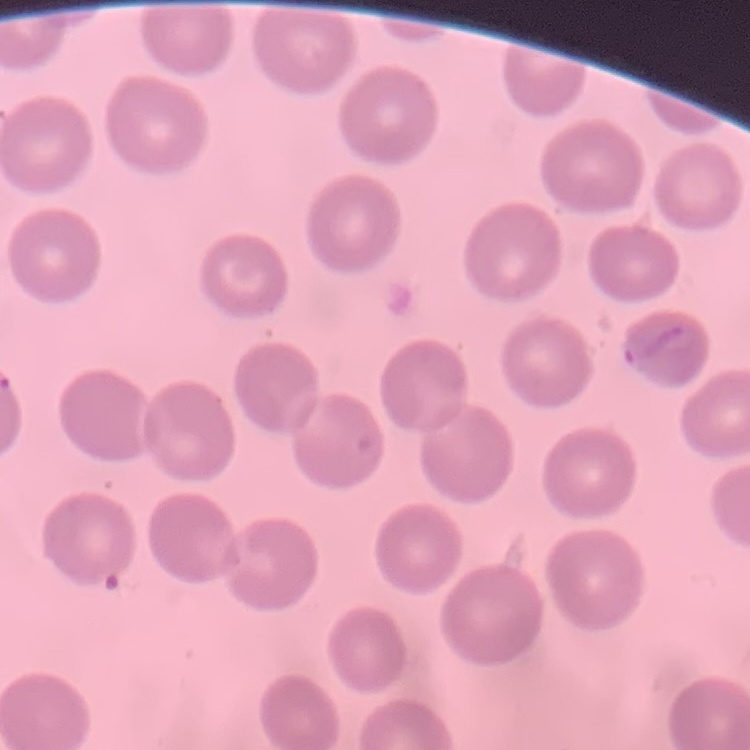
The erythrocytes exhibit no rouleaux formation. Thin blood film. One tile cut from a larger photomicrograph. Stained with either Field's or Giemsa.